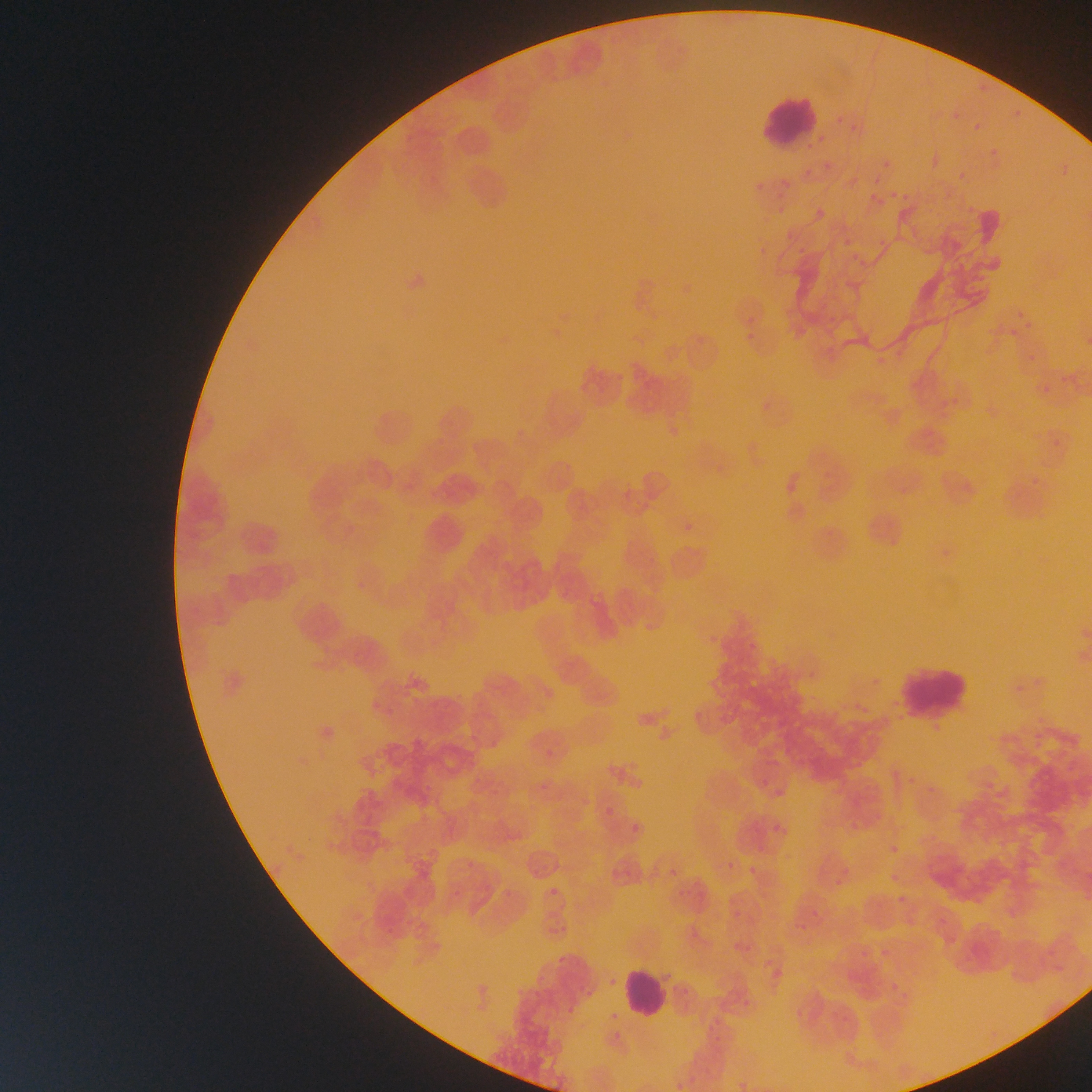
leukocyte locations = approximate bounding boxes as {left, top, right, bottom} in pixels: {753, 91, 822, 150}, {889, 662, 973, 717}, {620, 965, 670, 1020}
field of view = single
image size = 1092×1092 pixels
country = Ghana
capture = mobile-phone photograph through a microscope
preparation = thin blood smear
Plasmodium parasite locations = approximate bounding boxes as {left, top, right, bottom} in pixels: {973, 82, 985, 94}, {948, 105, 961, 124}, {1008, 105, 1025, 120}, {831, 111, 845, 122}, {843, 113, 872, 141}, {972, 120, 986, 134}, {986, 140, 1002, 159}, {826, 157, 838, 172}, {875, 159, 892, 180}, {1057, 159, 1067, 171}, {953, 172, 970, 188}, {889, 183, 905, 206}, {862, 187, 878, 202}, {778, 196, 791, 211}, {813, 208, 824, 220}, {787, 227, 795, 238}, {753, 242, 769, 261}, {1011, 304, 1024, 316}, {743, 313, 757, 327}, {1019, 322, 1037, 335}, {1010, 324, 1022, 341}, {739, 333, 755, 347}, {1025, 347, 1042, 366}, {1041, 380, 1051, 396}, {668, 417, 680, 432}, {681, 515, 698, 544}, {705, 632, 721, 649}, {364, 691, 382, 711}, {386, 698, 404, 716}, {929, 720, 942, 734}, {546, 749, 554, 757}, {907, 769, 921, 788}, {756, 779, 772, 791}, {774, 790, 788, 800}, {605, 807, 613, 816}, {849, 813, 863, 828}, {630, 817, 643, 834}, {772, 823, 780, 834}, {891, 835, 905, 856}, {727, 857, 736, 870}, {749, 865, 757, 875}, {666, 867, 678, 876}, {888, 870, 896, 883}, {831, 873, 843, 888}, {549, 888, 558, 896}, {894, 891, 904, 905}, {732, 912, 737, 920}, {794, 921, 807, 931}, {878, 943, 889, 959}, {856, 944, 866, 960}, {604, 974, 617, 989}, {887, 977, 899, 997}, {677, 987, 692, 998}, {797, 999, 811, 1017}, {741, 1001, 747, 1009} | approximate {x, y} pixel centers of objects too small to bound: {815, 913}